Report the malaria status of this cell.
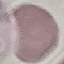

It is uninfected.

Summary:
  - Preparation: thin blood film
  - Capture: smartphone through the microscope eyepiece
  - Stain: Giemsa
  - Image type: cell patch, automatically extracted from a larger field of view and resized to 64 × 64 pixels